Describe the morphology of the erythrocytes.
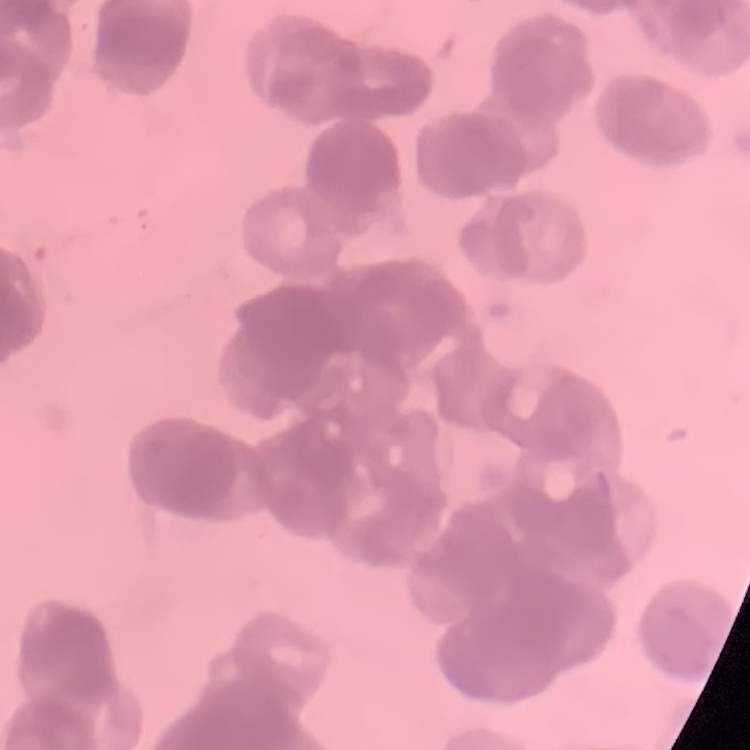

Rouleaux formation.

Thin blood smear. Field's or Giemsa stain. Square crop of a larger photomicrograph.